Name the parasite shown.
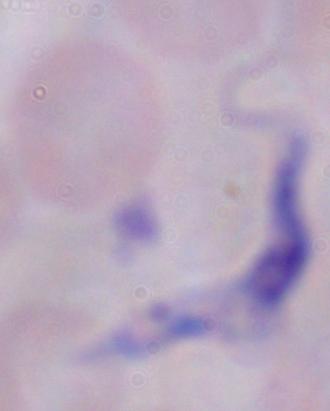
This is a trypanosome.

Captured at 1000x magnification. Photomicrograph.